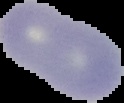
Result: no malaria parasites detected. Segmented cell region on a black background. Image is 124×103 pixels. From a thin blood smear.